Give the extent of all uninfected red blood cells.
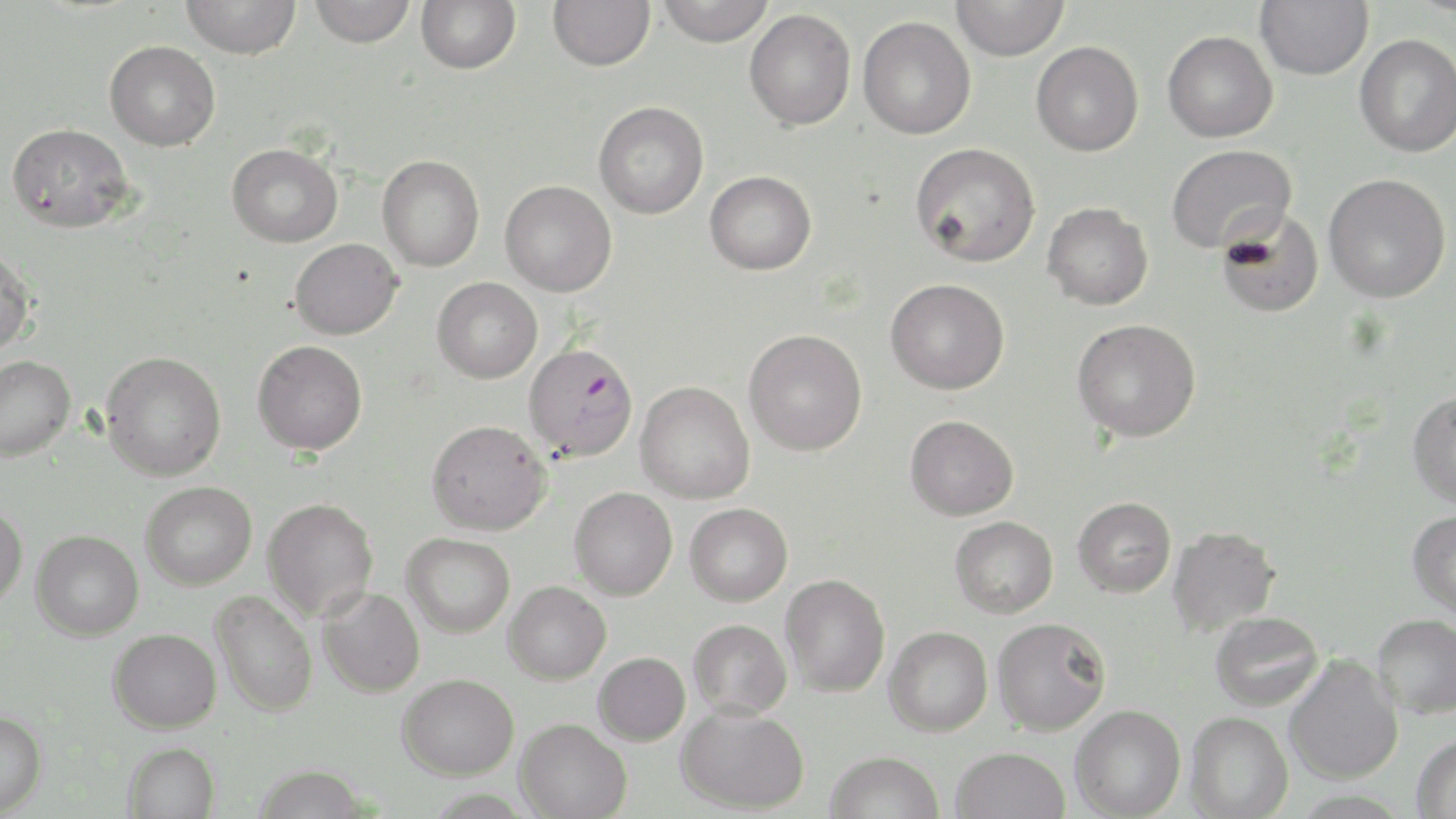
Approximate bounding boxes as [x1, y1, x2, y2] in pixels.
Uninfected red blood cells (subset): [181, 0, 301, 58], [309, 0, 416, 47], [415, 0, 521, 74], [548, 0, 655, 71], [655, 0, 775, 46], [951, 0, 1069, 60], [1255, 0, 1373, 80], [744, 9, 856, 131], [858, 15, 976, 139], [1162, 30, 1278, 142], [1355, 33, 1456, 157], [104, 40, 220, 151], [1030, 41, 1144, 156], [593, 101, 709, 219], [6, 122, 134, 233], [910, 142, 1041, 267], [227, 143, 342, 247], [1166, 143, 1296, 253], [377, 155, 484, 272], [704, 170, 816, 275], [1323, 173, 1451, 303], [500, 180, 617, 297], [1042, 202, 1153, 310], [1215, 206, 1324, 319], [289, 238, 402, 339], [0, 246, 36, 357], [432, 277, 542, 383], [885, 278, 1009, 394], [1072, 318, 1201, 442], [744, 328, 867, 456], [252, 340, 367, 455], [100, 351, 226, 480], [0, 355, 76, 461], [635, 381, 755, 504], [1407, 391, 1456, 509], [905, 415, 1019, 520], [427, 419, 551, 535], [140, 481, 257, 590], [569, 487, 678, 600], [1073, 496, 1176, 597], [263, 497, 378, 621], [0, 501, 28, 611], [684, 503, 793, 606], [1407, 510, 1456, 621], [950, 515, 1058, 618], [1167, 525, 1280, 636], [31, 529, 143, 641], [402, 532, 515, 638], [780, 574, 890, 697], [504, 581, 611, 684], [318, 587, 425, 698], [211, 589, 318, 717], [1210, 611, 1324, 711], [1372, 613, 1456, 719], [991, 617, 1111, 736], [688, 618, 792, 719], [884, 626, 993, 736], [108, 628, 222, 733], [593, 652, 690, 746], [1284, 654, 1403, 785], [398, 672, 519, 779], [676, 703, 809, 814], [1070, 705, 1186, 818], [0, 708, 48, 816], [1185, 711, 1292, 818], [515, 718, 631, 819], [1411, 732, 1456, 819], [123, 741, 220, 819], [951, 746, 1070, 819], [825, 751, 944, 819], [252, 764, 370, 818].

Slide-level diagnosis: Plasmodium falciparum. May-Grünwald-Giemsa stain. Image is 1456×819 pixels. Captured at 1000x magnification. Optical microscopy. Single field of view. Thin blood film.